Name the cell type shown.
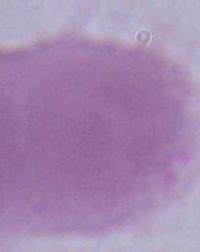

This is an erythrocyte.

modality = micrograph
magnification = 1000x